Report the malaria status of this cell.
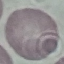
It is uninfected.

Summary:
  - Capture: smartphone through the microscope eyepiece
  - Stain: Giemsa
  - Preparation: thin blood film
  - Image type: cell patch, automatically extracted from a larger field of view and resized to 64 × 64 pixels